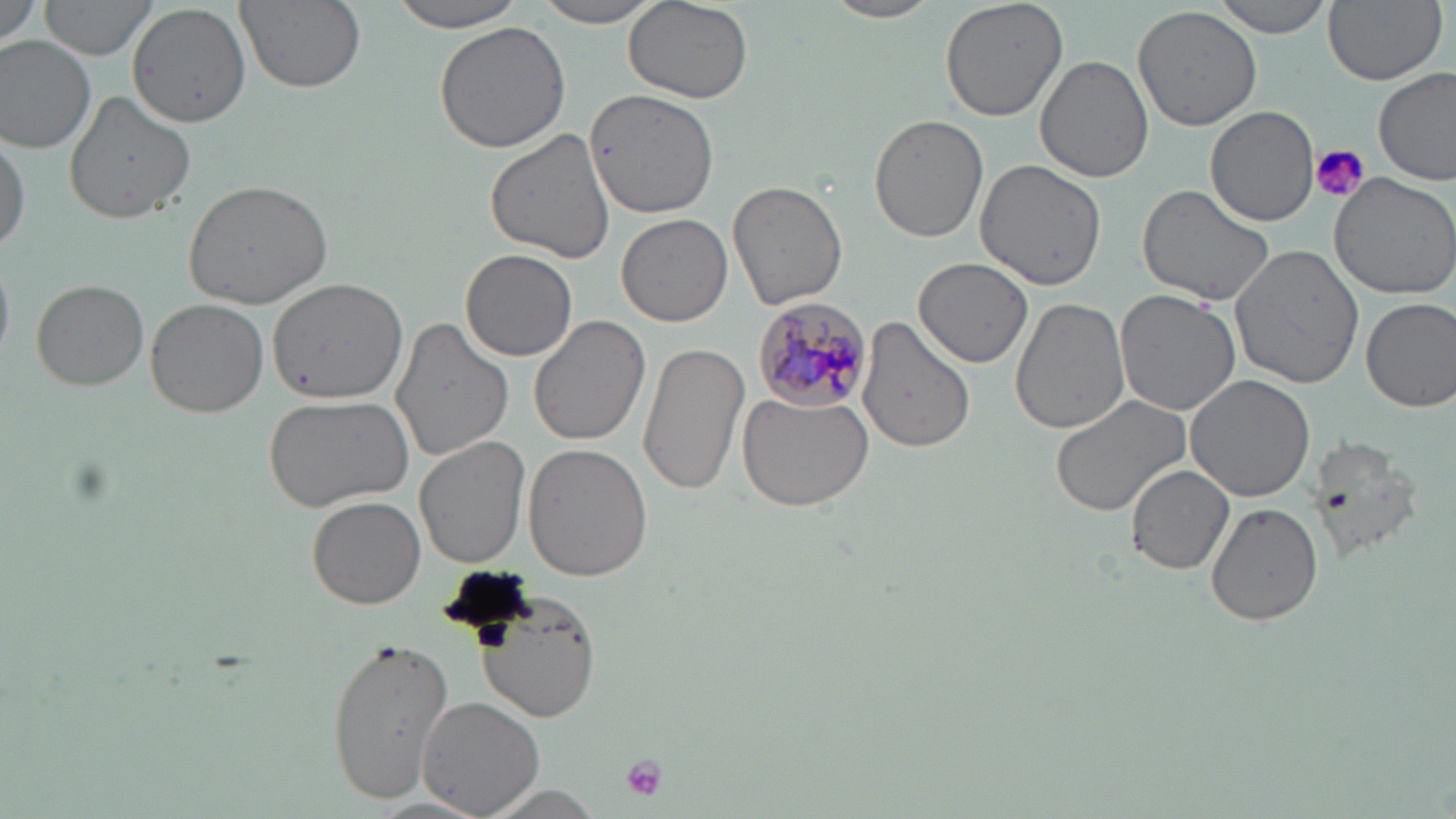

Summary:
  - Coordinate format: approximate bounding boxes as named x1/y1/x2/y2 corners in pixels
  - Plasmodium malariae-infected red blood cell locations: (x1=752, y1=295, x2=874, y2=410)
  - Uninfected red blood cell locations: (x1=1, y1=0, x2=45, y2=49), (x1=38, y1=0, x2=160, y2=62), (x1=234, y1=0, x2=365, y2=93), (x1=389, y1=0, x2=528, y2=32), (x1=531, y1=0, x2=666, y2=28), (x1=822, y1=0, x2=942, y2=24), (x1=940, y1=0, x2=1069, y2=122), (x1=1212, y1=0, x2=1333, y2=39), (x1=1322, y1=0, x2=1446, y2=86), (x1=624, y1=2, x2=754, y2=105), (x1=130, y1=4, x2=251, y2=127), (x1=1132, y1=5, x2=1263, y2=132), (x1=432, y1=19, x2=574, y2=155), (x1=0, y1=34, x2=97, y2=153), (x1=1035, y1=56, x2=1155, y2=183), (x1=1374, y1=67, x2=1455, y2=185), (x1=584, y1=89, x2=717, y2=218), (x1=64, y1=91, x2=196, y2=224), (x1=1206, y1=105, x2=1318, y2=224), (x1=870, y1=113, x2=989, y2=244), (x1=485, y1=128, x2=619, y2=265), (x1=0, y1=130, x2=28, y2=257), (x1=973, y1=158, x2=1107, y2=291), (x1=1327, y1=172, x2=1456, y2=300), (x1=182, y1=178, x2=333, y2=310), (x1=728, y1=178, x2=849, y2=311), (x1=1139, y1=184, x2=1278, y2=311), (x1=617, y1=213, x2=733, y2=327), (x1=1229, y1=244, x2=1364, y2=390), (x1=462, y1=250, x2=577, y2=361), (x1=913, y1=257, x2=1033, y2=366), (x1=268, y1=278, x2=409, y2=404), (x1=30, y1=280, x2=149, y2=392), (x1=1113, y1=289, x2=1241, y2=417), (x1=1009, y1=296, x2=1128, y2=435), (x1=1360, y1=296, x2=1456, y2=412), (x1=146, y1=300, x2=271, y2=418), (x1=528, y1=316, x2=649, y2=446), (x1=856, y1=316, x2=975, y2=457), (x1=390, y1=317, x2=514, y2=462), (x1=637, y1=341, x2=749, y2=497), (x1=1186, y1=374, x2=1314, y2=503), (x1=738, y1=389, x2=876, y2=512), (x1=262, y1=391, x2=414, y2=512), (x1=1050, y1=393, x2=1195, y2=518), (x1=1306, y1=435, x2=1424, y2=559), (x1=414, y1=436, x2=531, y2=569), (x1=523, y1=444, x2=653, y2=581), (x1=1127, y1=465, x2=1234, y2=574), (x1=306, y1=495, x2=425, y2=609), (x1=1207, y1=502, x2=1322, y2=626), (x1=478, y1=595, x2=601, y2=723), (x1=326, y1=634, x2=456, y2=805), (x1=417, y1=696, x2=547, y2=819), (x1=473, y1=784, x2=608, y2=819)
  - Platelet locations: (x1=1309, y1=143, x2=1369, y2=203), (x1=618, y1=753, x2=669, y2=801)
  - Slide-level diagnosis: Plasmodium malariae
  - Modality: light microscopy
  - Magnification: 1000x
  - Preparation: thin blood film
  - Field of view: one of a larger specimen
  - Image size: 1456×819 pixels
  - Stain: May-Grünwald-Giemsa